Give the position of every malaria parasite.
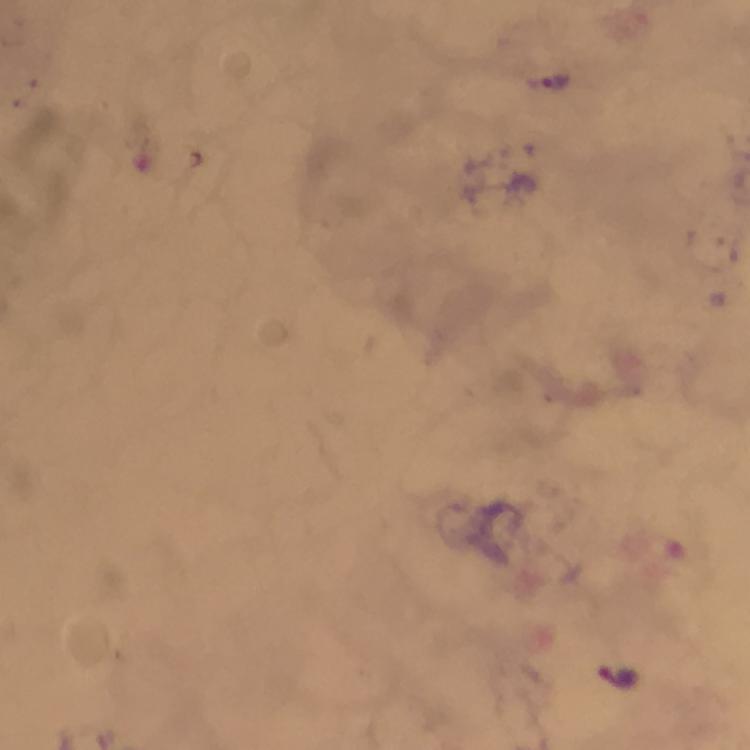
Approximate centers as {x, y} in pixels.
Malaria parasites: {551, 82}, {619, 677}.

{
  "stain": "Giemsa",
  "immersion_oil": "used",
  "context": "from a diagnostic examination for malaria",
  "preparation": "thick blood film",
  "magnification": "100x",
  "image_size": "750×750 pixels",
  "cropped_from": "one field of view",
  "capture": "smartphone photograph through a microscope"
}